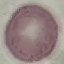

Summary:
  - Result: no malaria parasites seen
  - Preparation: thin smear
  - Image type: automatically extracted cell patch, resized to 64 × 64 pixels
  - Capture: smartphone through the microscope eyepiece
  - Stain: Giemsa